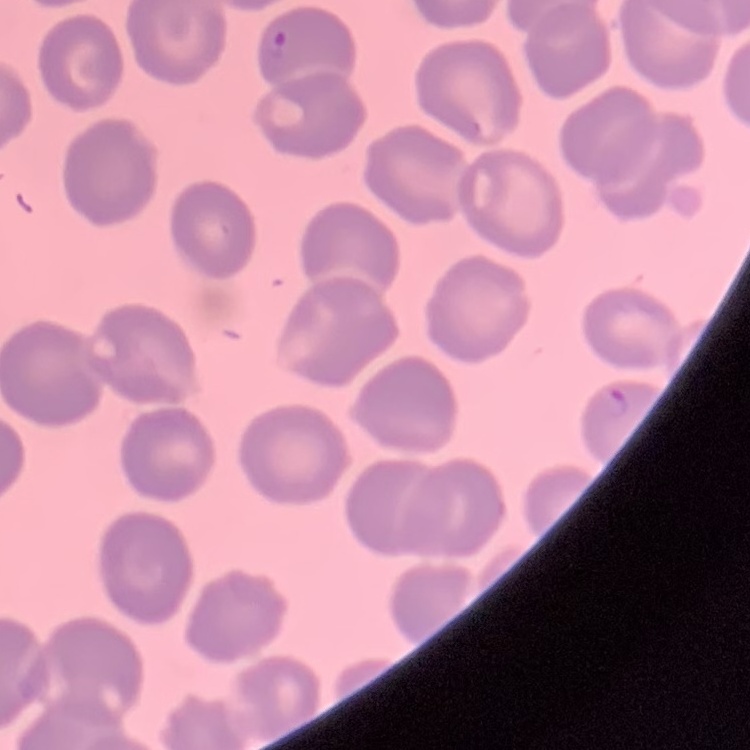 The red blood cells show no rouleaux formation. One tile cut from a larger photomicrograph. Field's or Giemsa stain. Thin blood film.